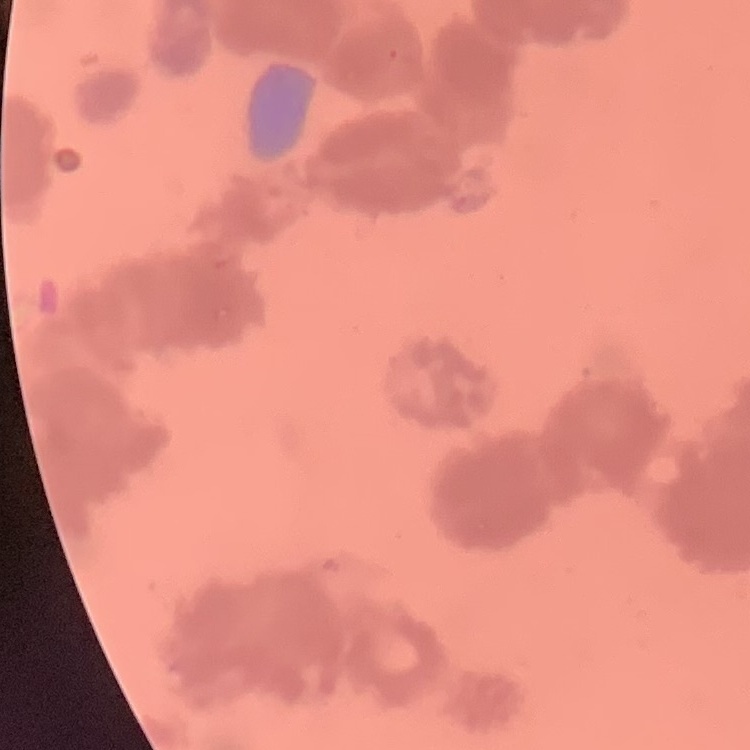

Summary:
  - Erythrocyte morphology: rouleaux formation
  - Image type: square crop of a larger photomicrograph
  - Preparation: thin blood film
  - Stain: Field's or Giemsa